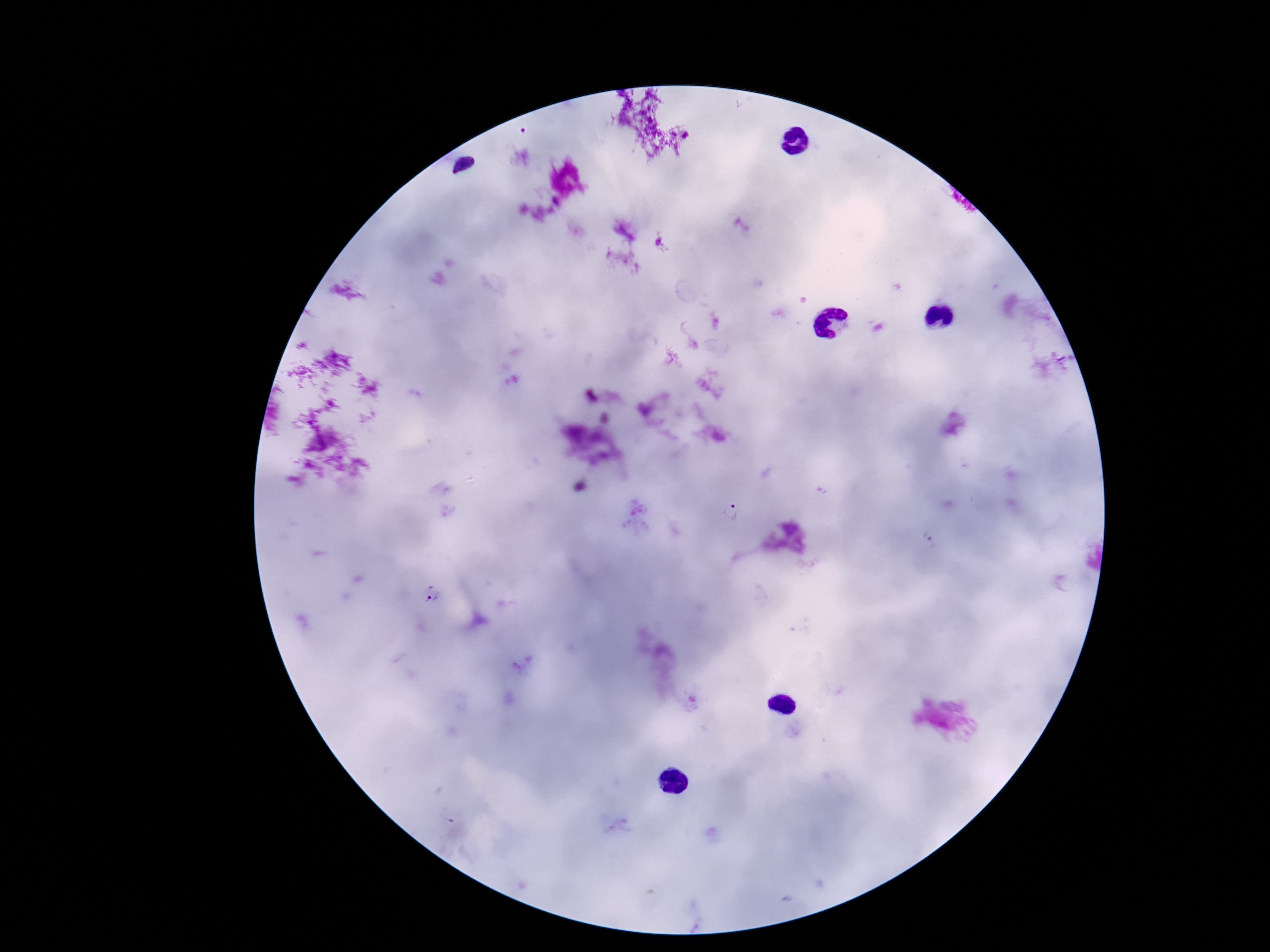

Plasmodium parasite locations = approximate centers as [x, y] in pixels: [733, 514], [432, 592]
stain = Giemsa
preparation = thick peripheral-blood smear
image size = 1270×952 pixels
field of view = one from this slide
patient malaria status = infected
capture = smartphone camera through the microscope eyepiece
magnification = 100x